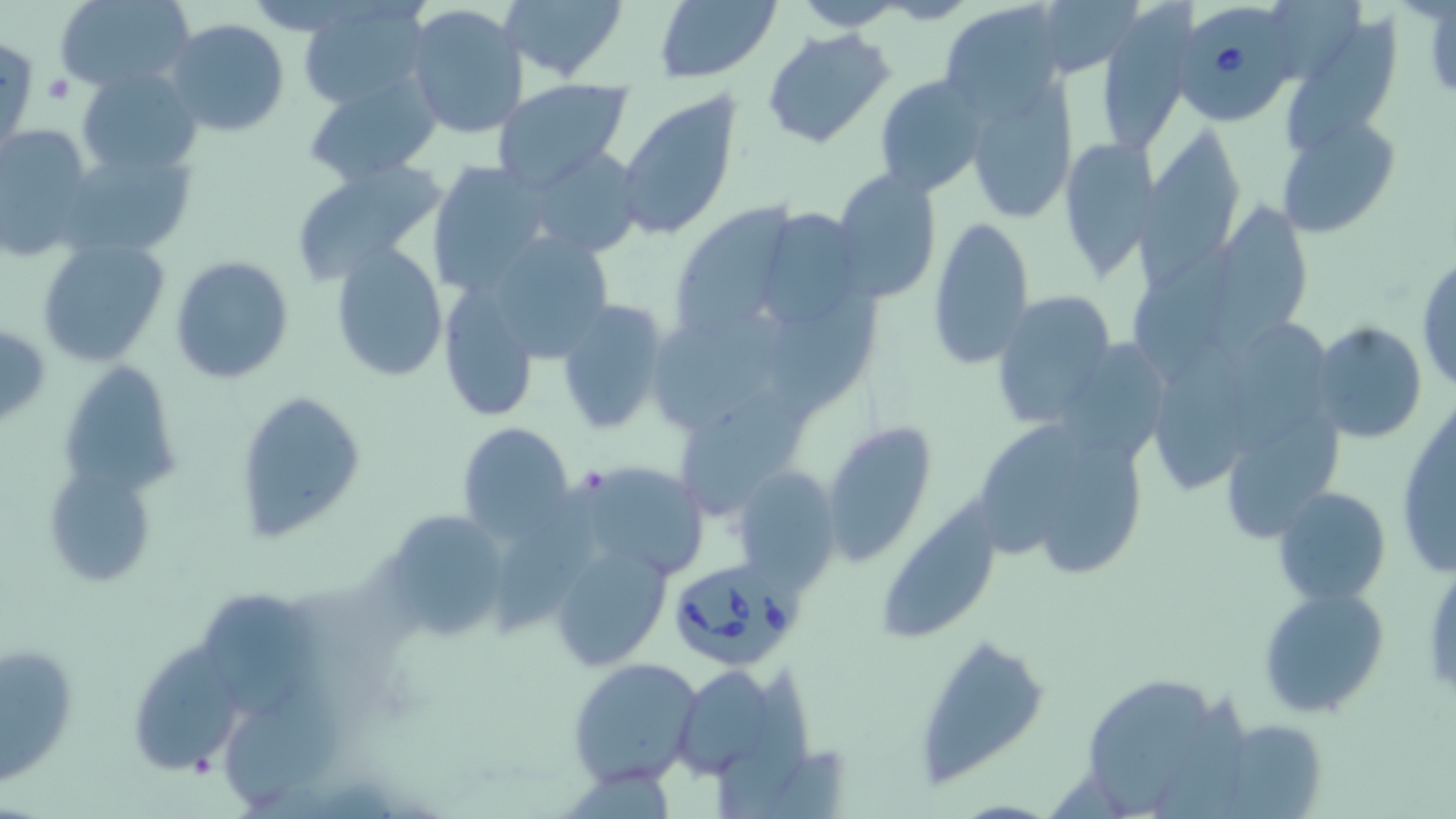
Summary:
  - Coordinate format: approximate bounding boxes as (x1,y1)-(x2,y2) corner pairs in pixels
  - Platelet locations: (43,74)-(73,103)
  - Babesia divergens-infected red blood cell locations: (1172,6)-(1293,125), (668,556)-(803,670)
  - Uninfected red blood cell locations: (53,0)-(196,94), (500,0)-(626,82), (790,0)-(912,31), (296,1)-(432,111), (653,2)-(780,82), (404,3)-(530,140), (939,3)-(1065,116), (1094,3)-(1199,155), (1282,9)-(1405,161), (165,17)-(291,136), (762,28)-(893,150), (0,35)-(38,155), (77,68)-(203,176), (959,69)-(1078,223), (872,72)-(991,198), (303,74)-(443,186), (491,79)-(632,190), (616,91)-(741,238), (1284,112)-(1398,240), (0,124)-(99,260), (1146,126)-(1243,265), (1057,135)-(1163,278), (61,142)-(199,262), (525,147)-(648,259), (287,158)-(450,286), (426,160)-(555,295), (831,168)-(942,302), (674,200)-(784,332), (1211,200)-(1322,366), (762,207)-(860,324), (926,214)-(1035,369), (495,230)-(614,365), (35,235)-(171,367), (1127,240)-(1242,382), (329,242)-(449,382), (1416,252)-(1455,394), (170,254)-(294,384), (437,281)-(545,422), (770,286)-(874,420), (990,290)-(1116,431), (551,298)-(671,436), (654,313)-(800,427), (1224,318)-(1332,455), (1311,321)-(1428,445), (1065,337)-(1170,458), (1156,339)-(1253,493), (58,358)-(180,496), (677,383)-(817,519), (234,387)-(368,543), (1395,393)-(1454,583), (1228,408)-(1342,545), (821,419)-(939,564), (977,420)-(1085,559), (457,422)-(575,541), (1037,436)-(1150,577), (572,459)-(711,583), (44,462)-(159,591), (731,467)-(841,593), (498,479)-(613,634), (1271,486)-(1393,606), (881,493)-(1007,637), (376,509)-(513,642), (547,537)-(672,671), (1258,586)-(1390,720), (204,591)-(324,719), (911,632)-(1047,783), (2,640)-(79,785), (140,642)-(247,776), (567,656)-(705,790), (666,660)-(795,778), (714,665)-(812,819), (230,675)-(352,804), (1084,677)-(1206,813), (1210,720)-(1326,819)
  - Slide-level diagnosis: Babesia divergens
  - Image size: 1456×819 pixels
  - Magnification: 1000x
  - Preparation: thin blood film
  - Field of view: one of a larger specimen
  - Stain: May-Grünwald-Giemsa
  - Modality: light microscopy